Name the parasite shown.
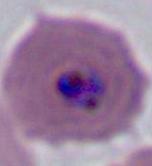

This is Plasmodium.

magnification: 400x or 1000x
modality: micrograph